Name the parasite shown.
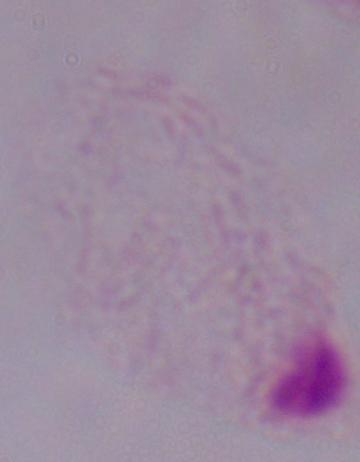
A trichomonad.

magnification = 1000x
modality = micrograph